State which parasite is depicted.
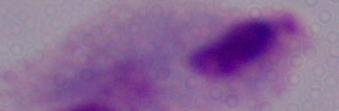

A trichomonad.

magnification = 1000x
modality = micrograph